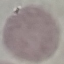
result: no malaria parasites detected
capture: smartphone through the microscope eyepiece
stain: Giemsa
image_type: cell patch, automatically extracted from a larger field of view and resized to 64 × 64 pixels
preparation: thin blood film